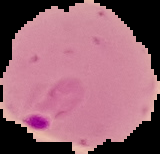
Summary:
  - Image size: 160×154 pixels
  - Result: Plasmodium parasites identified
  - Preparation: thin blood smear
  - Image type: segmented cell region with the area outside set to black